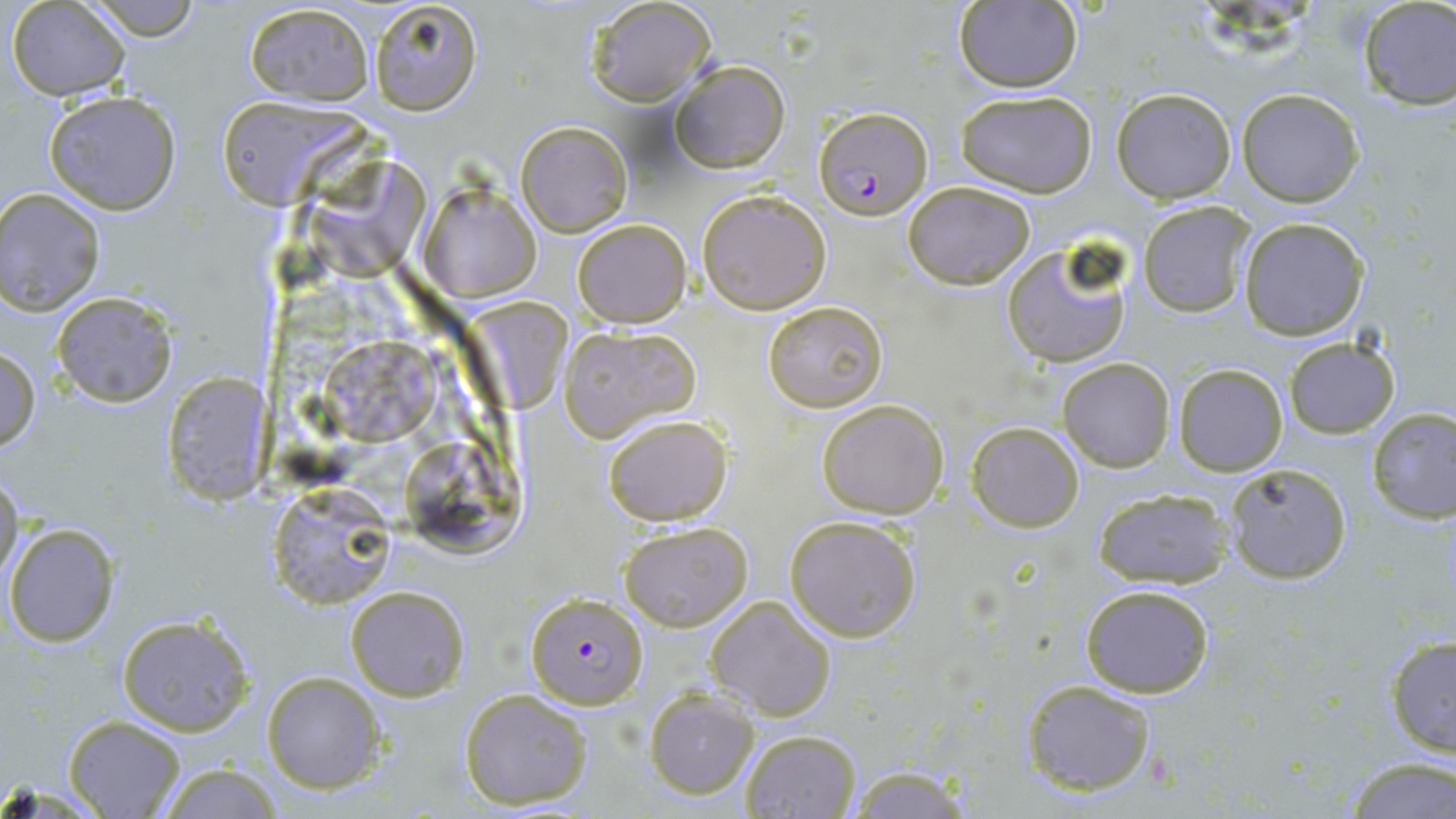
Approximate bounding boxes as named x1/y1/x2/y2 corners in pixels. Uninfected red blood cell locations: (x1=7, y1=0, x2=131, y2=100), (x1=85, y1=0, x2=202, y2=40), (x1=585, y1=0, x2=716, y2=108), (x1=367, y1=1, x2=484, y2=115), (x1=953, y1=2, x2=1083, y2=92), (x1=1356, y1=2, x2=1456, y2=111), (x1=244, y1=3, x2=374, y2=105), (x1=669, y1=59, x2=790, y2=173), (x1=1111, y1=88, x2=1235, y2=203), (x1=1237, y1=89, x2=1364, y2=206), (x1=956, y1=90, x2=1097, y2=197), (x1=44, y1=91, x2=182, y2=215), (x1=212, y1=93, x2=368, y2=207), (x1=515, y1=121, x2=631, y2=237), (x1=306, y1=149, x2=432, y2=281), (x1=903, y1=182, x2=1036, y2=289), (x1=421, y1=183, x2=540, y2=302), (x1=0, y1=187, x2=106, y2=318), (x1=697, y1=188, x2=831, y2=314), (x1=1138, y1=200, x2=1252, y2=317), (x1=1239, y1=217, x2=1369, y2=339), (x1=572, y1=218, x2=690, y2=328), (x1=1000, y1=241, x2=1135, y2=367), (x1=51, y1=292, x2=178, y2=407), (x1=457, y1=292, x2=572, y2=414), (x1=762, y1=299, x2=888, y2=413), (x1=558, y1=324, x2=699, y2=442), (x1=319, y1=333, x2=442, y2=443), (x1=1283, y1=335, x2=1399, y2=439), (x1=0, y1=347, x2=41, y2=454), (x1=1058, y1=357, x2=1174, y2=471), (x1=1173, y1=364, x2=1288, y2=475), (x1=161, y1=374, x2=275, y2=506), (x1=816, y1=400, x2=949, y2=518), (x1=1366, y1=405, x2=1456, y2=525), (x1=602, y1=414, x2=732, y2=526), (x1=966, y1=421, x2=1085, y2=532), (x1=397, y1=432, x2=528, y2=558), (x1=1223, y1=462, x2=1352, y2=585), (x1=0, y1=467, x2=23, y2=588), (x1=267, y1=485, x2=399, y2=607), (x1=1092, y1=487, x2=1235, y2=590), (x1=785, y1=514, x2=922, y2=642), (x1=619, y1=521, x2=753, y2=633), (x1=3, y1=522, x2=121, y2=647), (x1=1081, y1=583, x2=1214, y2=697), (x1=345, y1=585, x2=469, y2=700), (x1=707, y1=595, x2=836, y2=721), (x1=114, y1=612, x2=256, y2=737), (x1=1384, y1=634, x2=1456, y2=757), (x1=261, y1=671, x2=384, y2=794), (x1=1020, y1=679, x2=1157, y2=797), (x1=644, y1=686, x2=759, y2=800), (x1=459, y1=688, x2=595, y2=812), (x1=64, y1=716, x2=185, y2=818), (x1=737, y1=727, x2=862, y2=818), (x1=1340, y1=756, x2=1454, y2=819), (x1=155, y1=764, x2=285, y2=819), (x1=844, y1=765, x2=976, y2=819). Plasmodium falciparum-infected red blood cell locations: (x1=813, y1=105, x2=933, y2=220), (x1=525, y1=593, x2=648, y2=711). Slide-level diagnosis: Plasmodium falciparum. Single field of view. Light microscopy. Captured at 1000x magnification. Image is 1456×819 pixels. May-Grünwald-Giemsa-stained preparation. Thin blood film.